Classify this cell by malaria status.
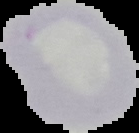

It is uninfected.

image type = cell region segmented out of the field of view; surrounding area masked to black
image size = 139×133 pixels
preparation = thin blood smear